Locate every malaria parasite and every leukocyte.
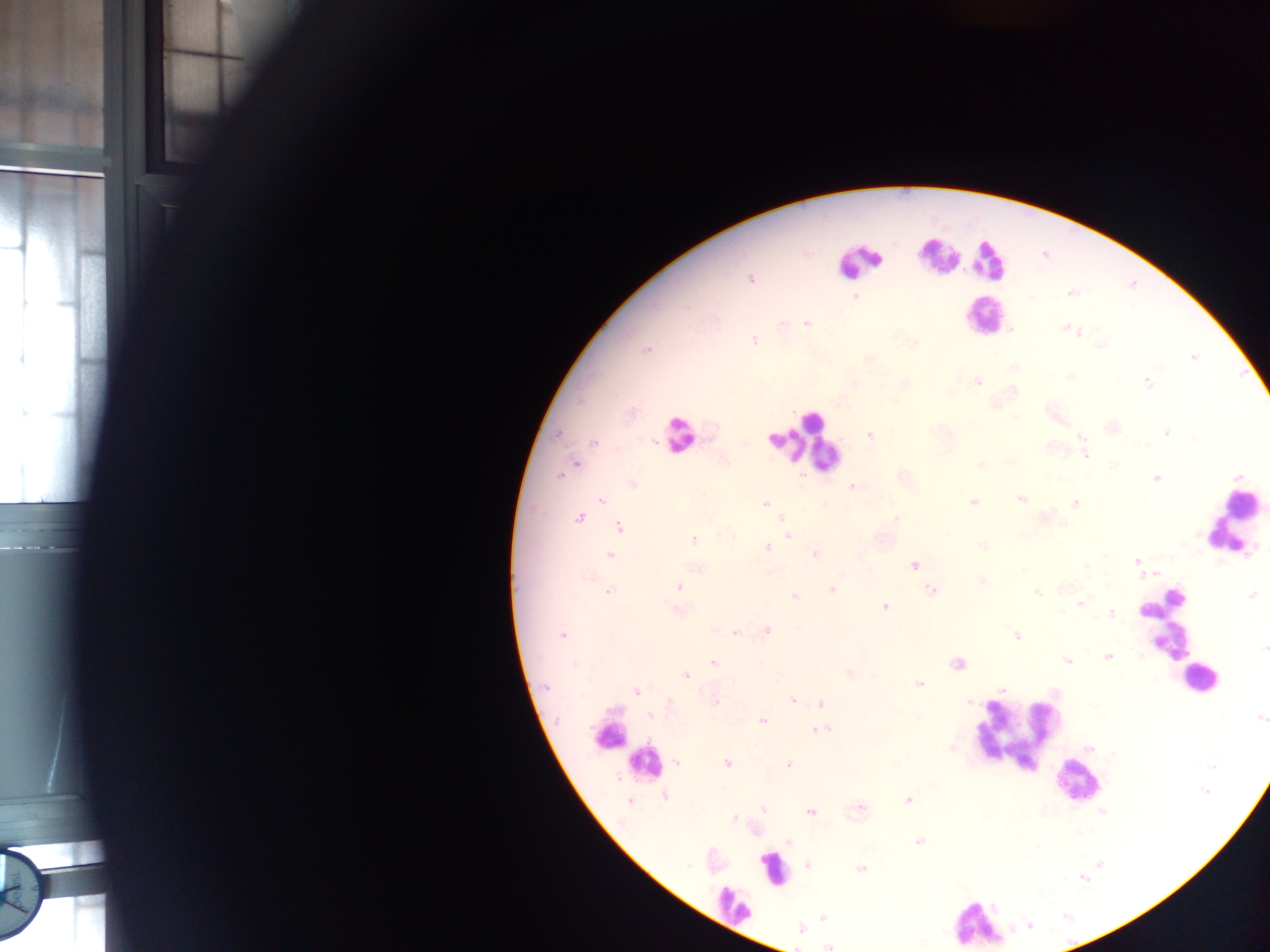

Approximate centers as [x, y] in pixels.
Malaria parasites: [920, 254], [751, 279], [1070, 293], [854, 297], [782, 323], [806, 323], [1065, 329], [1081, 332], [1075, 333], [754, 340], [1102, 345], [646, 350], [1194, 357], [869, 360], [1148, 382], [978, 383], [1013, 418], [1167, 432], [869, 434], [1081, 438], [593, 441], [1084, 451], [1085, 455], [576, 463], [1010, 463], [980, 464], [557, 475], [1155, 480], [632, 484], [852, 487], [600, 500], [1021, 500], [766, 503], [973, 503], [1075, 503], [579, 517], [781, 518], [896, 518], [618, 527], [788, 536], [694, 538], [982, 545], [767, 548], [814, 554], [610, 555], [1136, 560], [914, 566], [1085, 567], [1024, 570], [1140, 573], [982, 581], [679, 587], [831, 589], [930, 591], [610, 592], [1037, 593], [794, 596], [1081, 604], [885, 608], [679, 611], [1142, 611], [1111, 615], [714, 629], [767, 630], [736, 632], [562, 635], [1017, 637], [1261, 647], [1107, 656], [1068, 661], [712, 662], [958, 663], [573, 664], [849, 673], [686, 675], [919, 686], [545, 688], [1000, 690], [638, 692], [792, 700], [716, 701], [977, 702], [669, 703], [820, 703], [651, 715], [763, 719], [1259, 719], [557, 720], [817, 730], [826, 730], [726, 763], [676, 764], [789, 764], [663, 797], [908, 799], [630, 801], [860, 807], [763, 811], [810, 813], [733, 818], [918, 841], [790, 843], [762, 859], [807, 865], [861, 868], [1083, 880], [22, 893], [823, 917], [801, 928], [829, 946].
Leukocytes: [982, 257], [853, 270], [974, 316], [677, 440], [807, 451], [1234, 522], [1194, 688], [1012, 738], [604, 740], [650, 762], [1079, 794], [729, 908], [975, 926].

One field of view. Collected in Ghana. Mobile-phone photograph taken through the microscope. Thick blood film. Image is 1270×952 pixels.